Locate and identify every blood parasite.
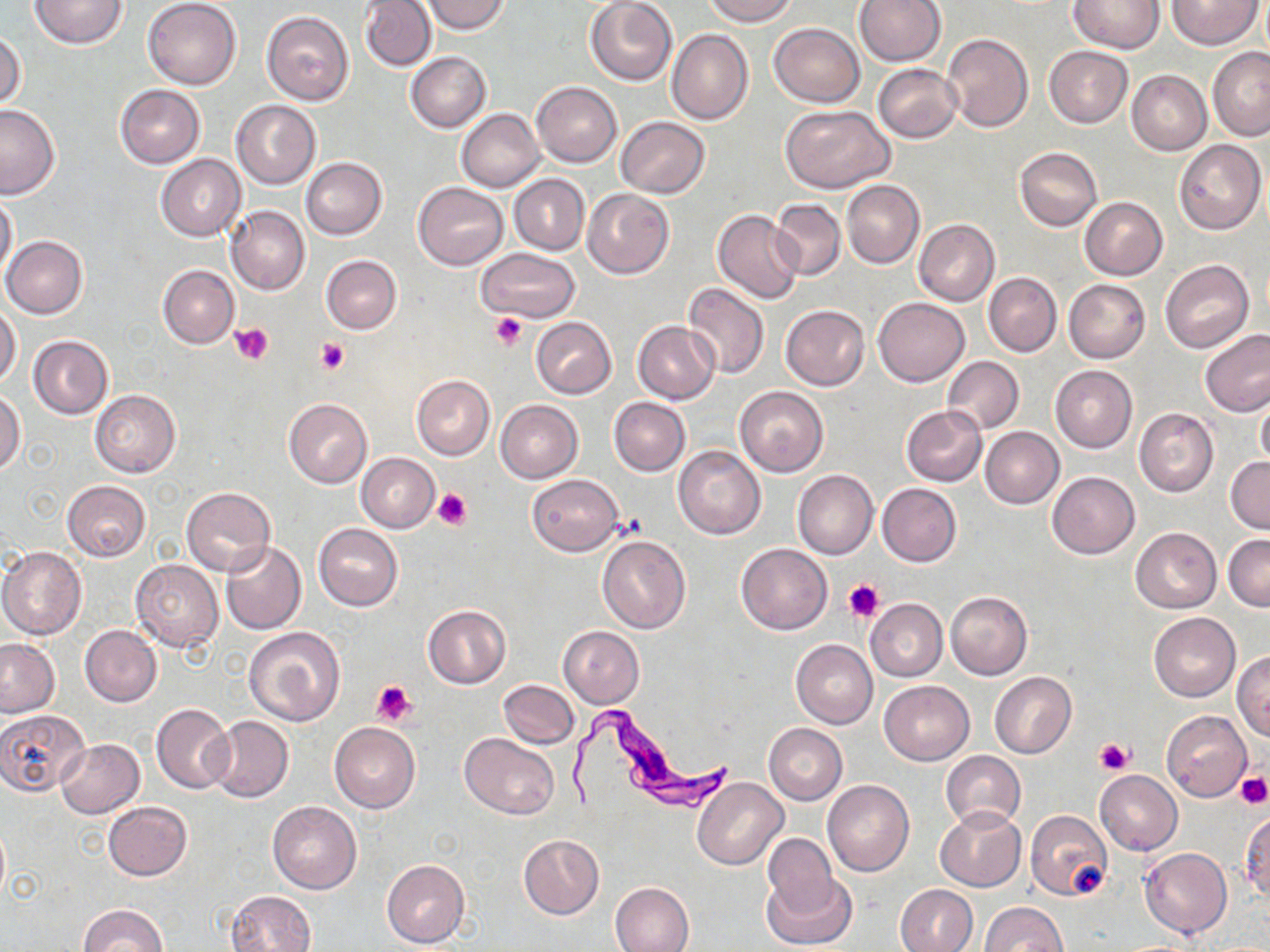

Approximate bounding boxes as (x1, y1, x2, y2) in pixels.
Trypanosoma brucei: (568, 702, 737, 814).
No Plasmodium falciparum, Plasmodium ovale, Plasmodium malariae, Plasmodium vivax, or Babesia divergens observed.

slide_level_diagnosis: Trypanosoma brucei
magnification: 1000x
platelet_locations: 'approximate bounding boxes as (x1, y1, x2, y2) in pixels: (491, 313, 526, 349), (230, 323, 273, 365), (315, 337, 351, 375), (433, 488, 470, 531), (843, 578, 884, 622), (372, 680, 416, 728), (1094, 738, 1133, 776), (1234, 772, 1270, 808), (1071, 862, 1110, 898)'
preparation: thin blood smear
modality: light microscopy
uninfected_red_blood_cell_locations: 'approximate bounding boxes as (x1, y1, x2, y2) in pixels: (29, 0, 127, 49), (144, 0, 242, 88), (421, 0, 510, 33), (703, 0, 798, 25), (854, 0, 945, 67), (1167, 0, 1263, 49), (360, 1, 437, 71), (585, 1, 677, 85), (1069, 1, 1165, 54), (261, 11, 355, 105), (769, 23, 865, 107), (667, 29, 752, 125), (0, 31, 25, 112), (942, 34, 1033, 132), (1043, 45, 1133, 128), (1208, 47, 1270, 139), (406, 52, 490, 132), (872, 64, 962, 142), (1126, 70, 1211, 155), (532, 81, 622, 167), (115, 85, 204, 167), (231, 100, 320, 189), (0, 104, 60, 198), (781, 105, 893, 193), (457, 109, 545, 191), (615, 116, 710, 198), (1174, 139, 1266, 234), (1014, 147, 1102, 231), (155, 154, 246, 240), (300, 157, 387, 239), (509, 174, 589, 255), (842, 180, 925, 269), (413, 182, 508, 270), (582, 188, 675, 279), (0, 191, 18, 284), (1080, 197, 1167, 280), (770, 199, 846, 280), (227, 205, 309, 296), (713, 210, 804, 305), (914, 219, 999, 306), (2, 235, 87, 319), (477, 248, 580, 324), (321, 255, 401, 334), (1160, 260, 1253, 351), (157, 265, 238, 348), (984, 272, 1061, 357), (1064, 279, 1150, 362), (684, 282, 769, 379), (873, 297, 969, 386), (0, 302, 21, 390), (781, 304, 869, 390), (531, 317, 617, 398), (632, 321, 720, 404), (1199, 328, 1270, 418), (28, 335, 113, 419), (942, 356, 1023, 434), (1051, 366, 1136, 452), (411, 374, 495, 460), (735, 386, 829, 478), (1, 389, 25, 476), (89, 390, 180, 476), (1256, 393, 1270, 470), (609, 397, 690, 476), (283, 398, 372, 487), (496, 399, 583, 483), (901, 405, 988, 486), (1134, 408, 1218, 497), (980, 427, 1064, 508), (674, 446, 765, 540), (356, 453, 439, 532), (1226, 456, 1270, 534), (792, 470, 878, 559), (1047, 471, 1139, 558), (527, 474, 623, 556), (62, 480, 151, 562), (877, 483, 961, 566), (181, 486, 275, 577), (313, 523, 403, 610), (1131, 526, 1222, 612), (1223, 533, 1270, 609), (597, 535, 690, 633), (220, 541, 305, 635), (736, 543, 832, 635), (1, 546, 86, 640), (131, 560, 223, 652), (945, 590, 1032, 679), (865, 598, 947, 681), (422, 605, 510, 689), (1149, 612, 1240, 702), (80, 624, 162, 706), (244, 625, 345, 726), (557, 626, 645, 707), (0, 639, 59, 716), (791, 640, 877, 729), (1233, 651, 1270, 741), (989, 671, 1076, 757), (498, 679, 578, 749), (879, 680, 974, 765), (151, 703, 234, 794), (0, 708, 90, 797), (1162, 711, 1252, 800), (207, 716, 293, 803), (329, 723, 421, 812), (764, 724, 847, 805), (461, 733, 558, 818), (56, 737, 144, 818), (941, 751, 1026, 831), (1095, 770, 1183, 856), (692, 777, 787, 869), (822, 781, 914, 877), (103, 801, 192, 880), (268, 801, 361, 894), (936, 807, 1025, 891), (1025, 811, 1112, 901), (1241, 812, 1270, 902), (518, 834, 603, 919), (762, 834, 840, 917), (1139, 847, 1232, 938), (381, 858, 469, 948), (764, 870, 855, 949), (611, 881, 695, 952), (895, 884, 978, 952), (227, 889, 316, 952), (980, 901, 1066, 951), (78, 905, 166, 952)'
image_size: 1270×952 pixels
field_of_view: one of a larger specimen
stain: May-Grünwald-Giemsa